Evaluate for malaria.
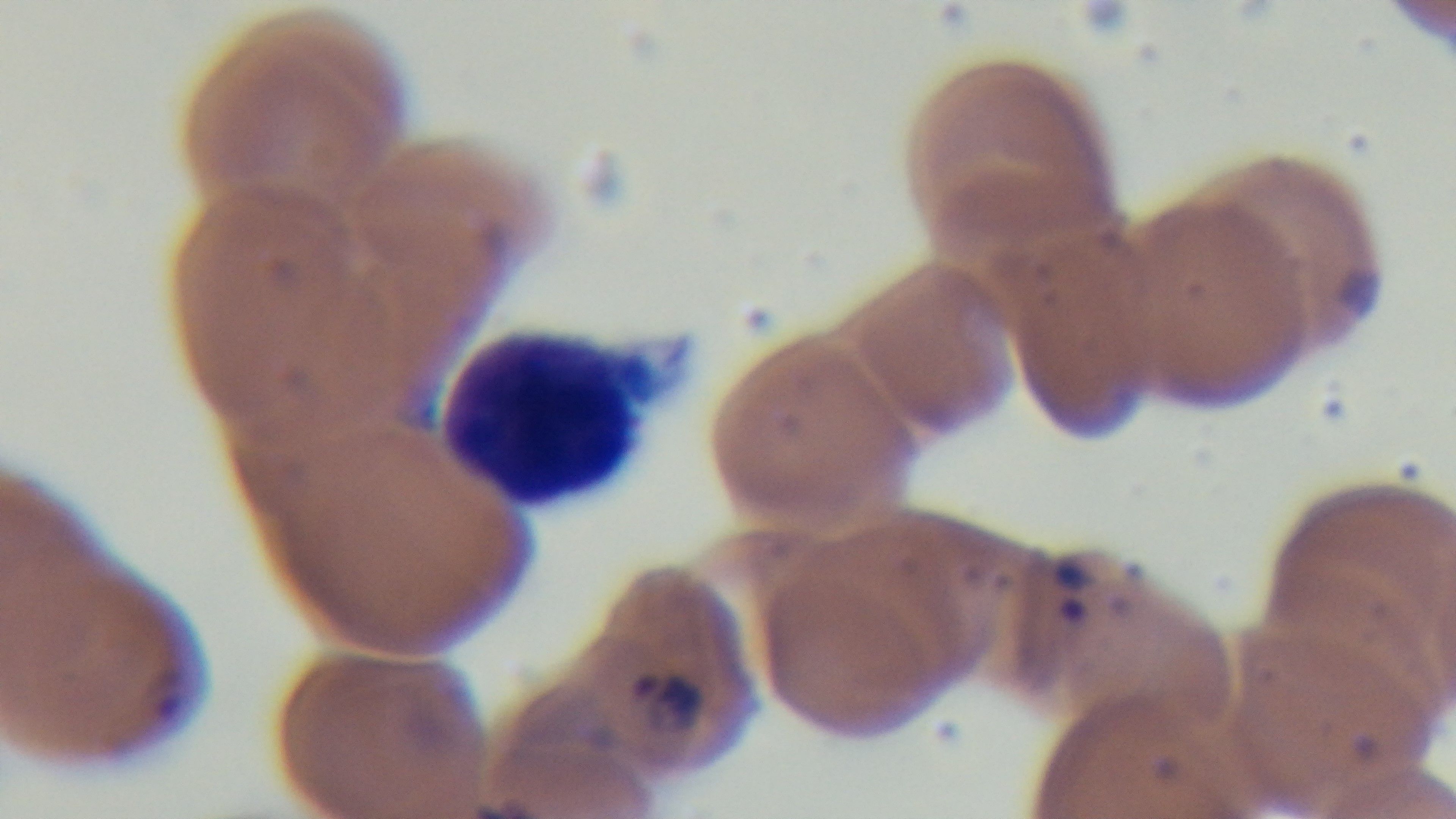
Infected.

{
  "capture": "mounted 4K digital camera",
  "modality": "light microscopy",
  "objective": "100x oil immersion",
  "stain": "Giemsa",
  "field_of_view": "one from the slide",
  "preparation": "thin"
}